Assess the morphology of the red blood cells.
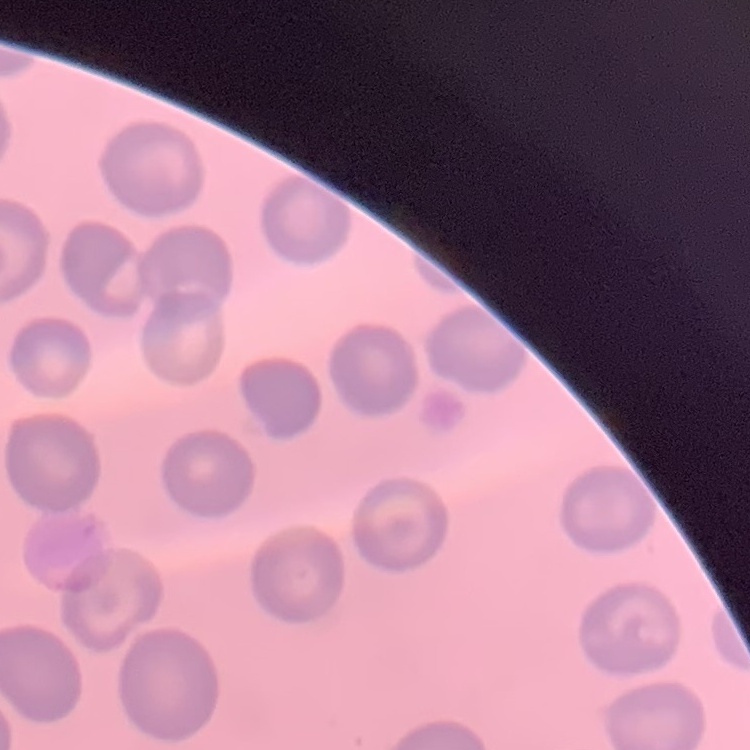
They show no rouleaux formation.

stain = Field's or Giemsa
image type = square crop of a larger photomicrograph
preparation = thin blood film